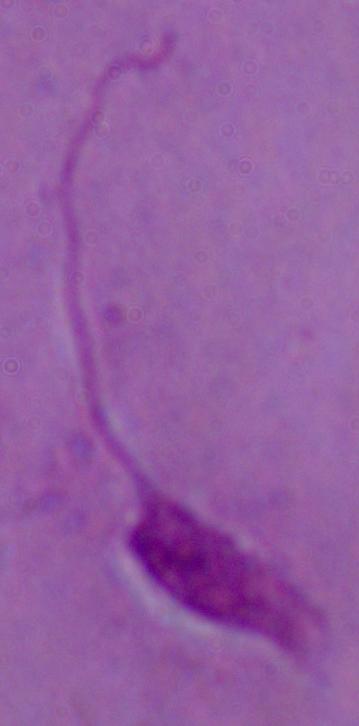
modality = micrograph
identification = Leishmania
magnification = 1000x